Name the parasite shown.
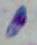
Toxoplasma gondii.

Summary:
  - Modality: photomicrograph
  - Magnification: 1000x